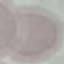

Malaria status: uninfected. Acquired by smartphone through the microscope eyepiece. Automatically extracted cell patch, resized to 64 × 64 pixels. Giemsa stain. Thin blood film.